Classify this cell by malaria status.
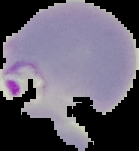
Parasitized.

Summary:
  - Preparation: thin blood film
  - Image type: segmented cell region with the area outside set to black
  - Image size: 139×151 pixels